Identify the parasite.
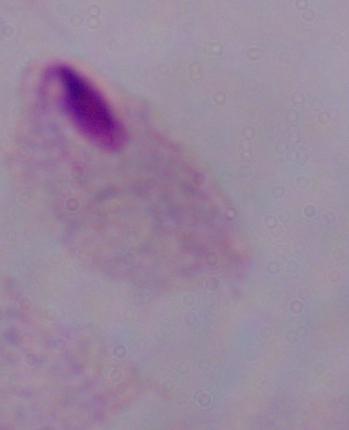

A trichomonad.

Summary:
  - Magnification: 1000x
  - Modality: micrograph